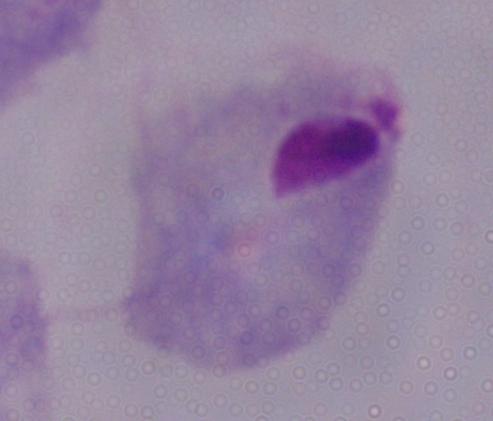
modality = photomicrograph
magnification = 1000x
identification = trichomonad